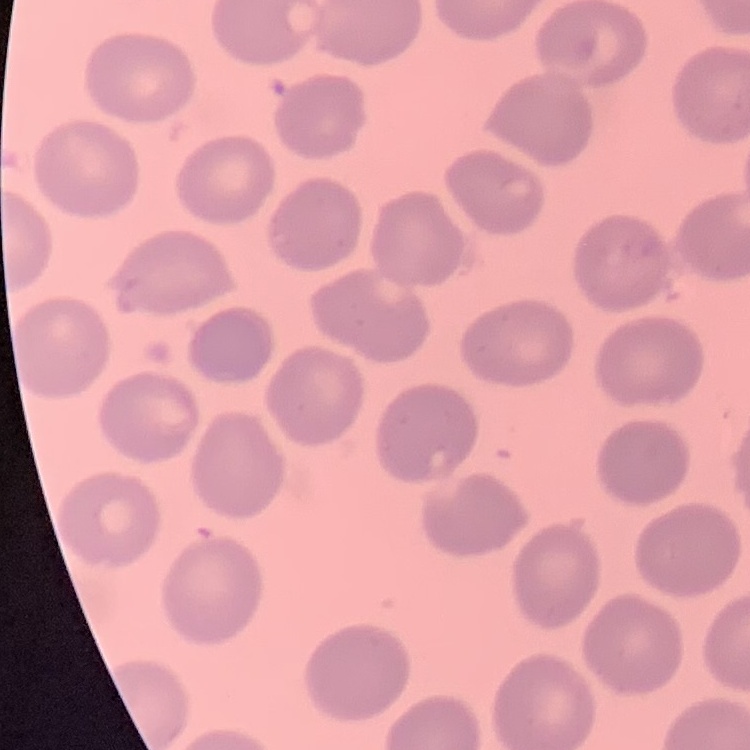
red blood cell morphology = no rouleaux formation
stain = Field's or Giemsa
preparation = thin peripheral smear
image type = one tile cut from a larger photomicrograph